Identify the parasite.
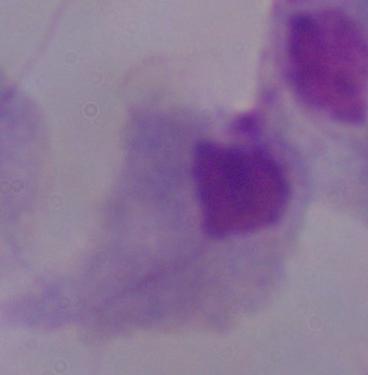
A trichomonad.

1000x magnification. Micrograph.